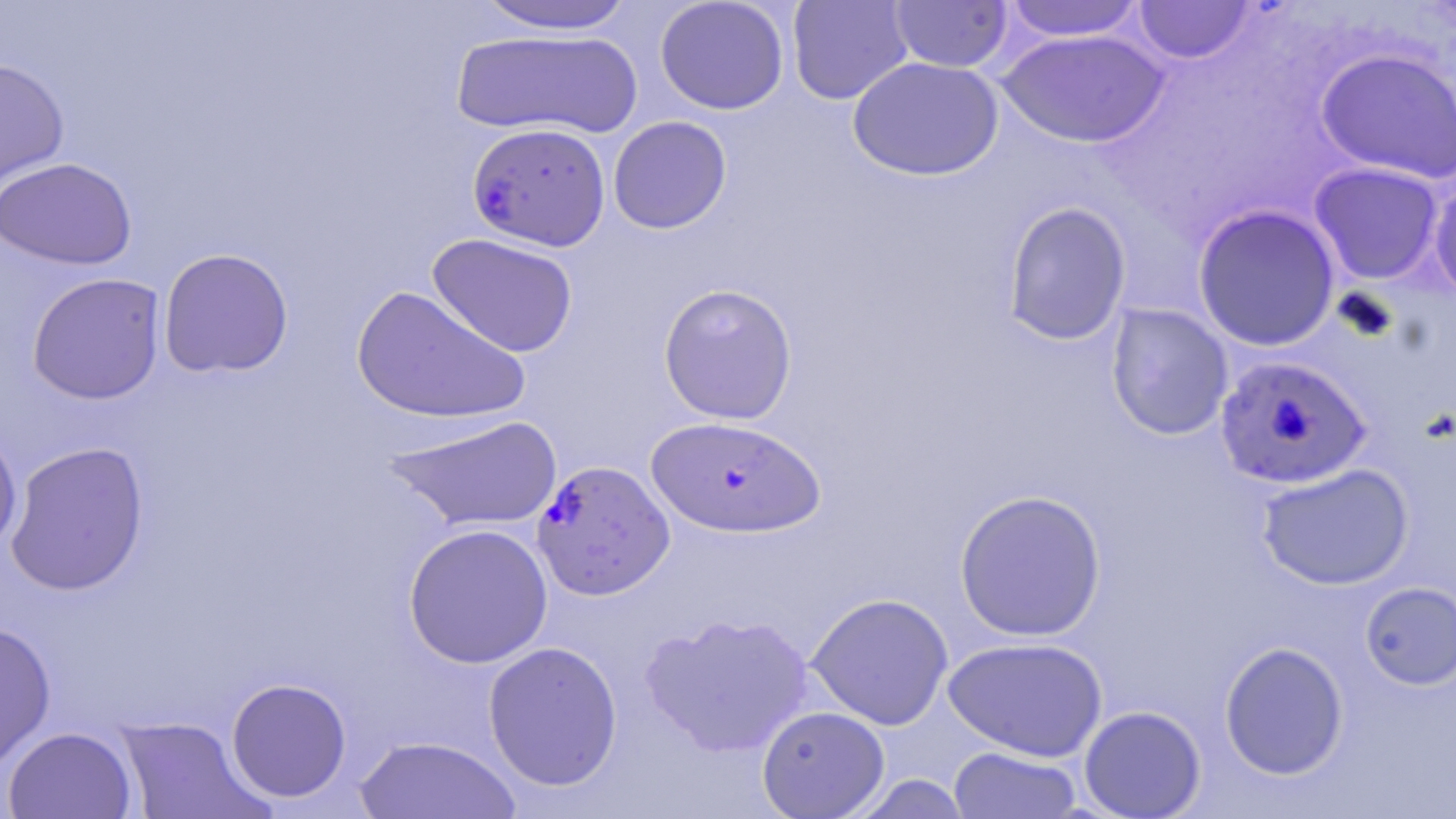

Approximate bounding boxes as (x1, y1, x2, y2) in pixels. Uninfected red blood cell locations: (655, 0, 790, 115), (787, 0, 913, 105), (1003, 0, 1148, 42), (1133, 0, 1257, 65), (472, 1, 642, 35), (888, 1, 1013, 73), (449, 29, 644, 139), (998, 29, 1170, 148), (1315, 48, 1456, 184), (847, 56, 1004, 180), (0, 57, 69, 195), (608, 116, 732, 234), (0, 157, 138, 271), (1308, 162, 1444, 285), (1429, 172, 1456, 304), (1001, 200, 1132, 346), (1193, 204, 1341, 351), (427, 233, 579, 358), (157, 247, 294, 378), (26, 272, 166, 405), (658, 282, 798, 424), (350, 285, 532, 425), (1105, 303, 1234, 441), (384, 413, 564, 533), (0, 423, 23, 556), (4, 441, 150, 597), (1256, 462, 1414, 590), (954, 488, 1107, 642), (403, 523, 553, 669), (1359, 581, 1456, 690), (806, 592, 953, 730), (640, 611, 815, 758), (0, 621, 56, 772), (942, 637, 1108, 762), (482, 641, 623, 791), (1219, 641, 1349, 780), (225, 677, 352, 803), (757, 705, 890, 817), (1079, 705, 1206, 818), (115, 715, 267, 819), (2, 726, 138, 819), (355, 735, 523, 819), (948, 746, 1082, 818), (847, 774, 974, 818). Plasmodium falciparum-infected red blood cell locations: (467, 122, 611, 251), (1214, 354, 1372, 489), (645, 416, 826, 538), (532, 459, 675, 600). Slide-level diagnosis: Plasmodium falciparum. Image is 1456×819 pixels. Light microscopy. Captured at 1000x magnification. Thin blood film. May-Grünwald-Giemsa stain. One field of a larger specimen.